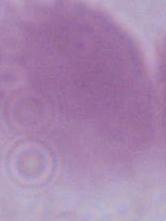

Summary:
  - Modality: micrograph
  - Identification: red blood cell
  - Magnification: 1000x